Report the malaria status.
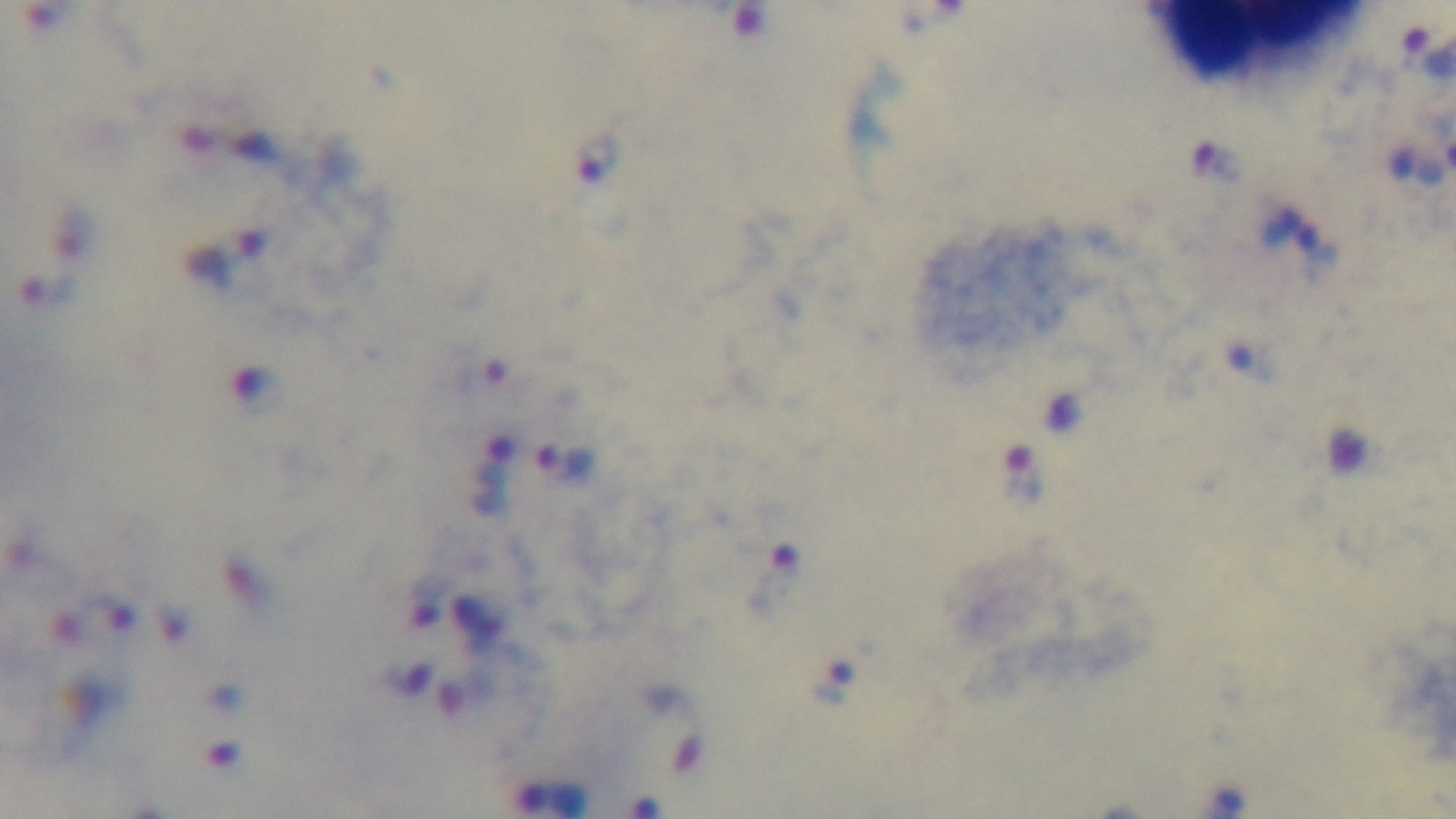

Positive.

One field from the slide. Captured with a mounted 4K digital camera. Giemsa-stained. Photomicrograph. Oil-immersion objective, 100x. Preparation: thick blood film.